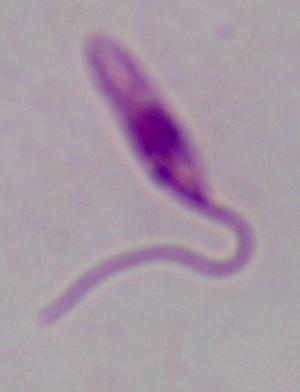 Captured at 1000x magnification. Micrograph. A Leishmania parasite is seen.